Assess this cell for malaria.
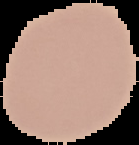
It is uninfected.

image size = 139×145 pixels
image type = cell region segmented out of the field of view; surrounding area masked to black
preparation = thin blood film